Give the extent of all Trypanosoma brucei.
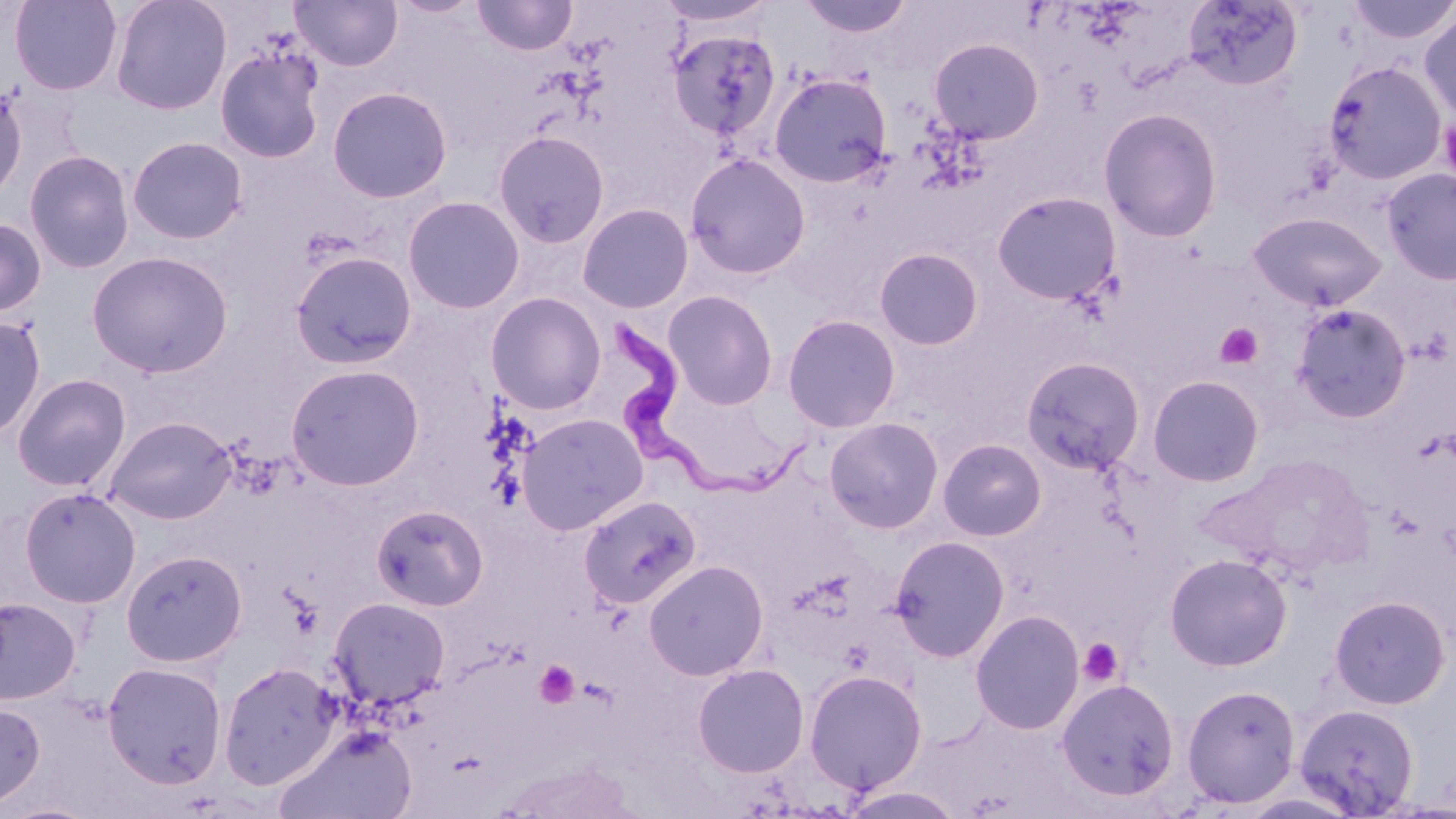

Approximate bounding boxes as [x1, y1, x2, y2] in pixels.
Trypanosoma brucei: [605, 312, 818, 509].

slide_level_diagnosis: Trypanosoma brucei
platelet_locations: 'approximate bounding boxes as [x1, y1, x2, y2] in pixels: [1440, 115, 1456, 188], [1215, 324, 1263, 369], [1077, 638, 1124, 688], [534, 660, 580, 708]'
magnification: 1000x
image_size: 1456×819 pixels
preparation: thin blood smear
uninfected_red_blood_cell_locations: 'approximate bounding boxes as [x1, y1, x2, y2] in pixels: [10, 0, 123, 95], [110, 0, 232, 115], [290, 0, 403, 71], [472, 0, 577, 56], [797, 0, 914, 39], [1181, 0, 1304, 91], [1344, 0, 1456, 44], [1419, 9, 1456, 125], [667, 29, 781, 143], [928, 38, 1044, 144], [214, 44, 327, 164], [1323, 59, 1447, 185], [769, 72, 893, 188], [326, 85, 453, 203], [0, 86, 27, 201], [1098, 108, 1223, 242], [492, 130, 610, 248], [127, 136, 248, 244], [23, 149, 135, 273], [684, 152, 811, 279], [1380, 167, 1456, 285], [992, 191, 1122, 304], [403, 195, 525, 314], [577, 203, 694, 313], [1248, 211, 1387, 311], [0, 217, 46, 318], [874, 247, 984, 351], [87, 250, 233, 378], [290, 250, 417, 369], [662, 290, 779, 410], [485, 292, 607, 414], [1291, 303, 1412, 423], [781, 314, 901, 433], [0, 315, 46, 441], [1021, 356, 1146, 475], [285, 364, 425, 490], [12, 373, 131, 491], [1147, 375, 1265, 487], [516, 413, 649, 535], [104, 415, 237, 525], [824, 417, 944, 534], [937, 438, 1046, 541], [19, 487, 141, 608], [578, 494, 702, 608], [371, 503, 489, 611], [889, 535, 1010, 662], [120, 548, 247, 667], [1163, 552, 1293, 671], [643, 559, 769, 681], [1328, 594, 1452, 710], [328, 596, 450, 711], [0, 598, 80, 705], [969, 609, 1085, 735], [102, 661, 226, 789], [218, 662, 342, 790], [692, 663, 810, 778], [804, 669, 928, 793], [1055, 678, 1180, 802], [1181, 683, 1301, 808], [0, 701, 46, 808], [1293, 702, 1419, 816], [275, 727, 419, 819], [837, 784, 966, 818], [0, 801, 102, 818]'
stain: May-Grünwald-Giemsa
field_of_view: single
modality: optical microscopy